Locate and identify every blood parasite.
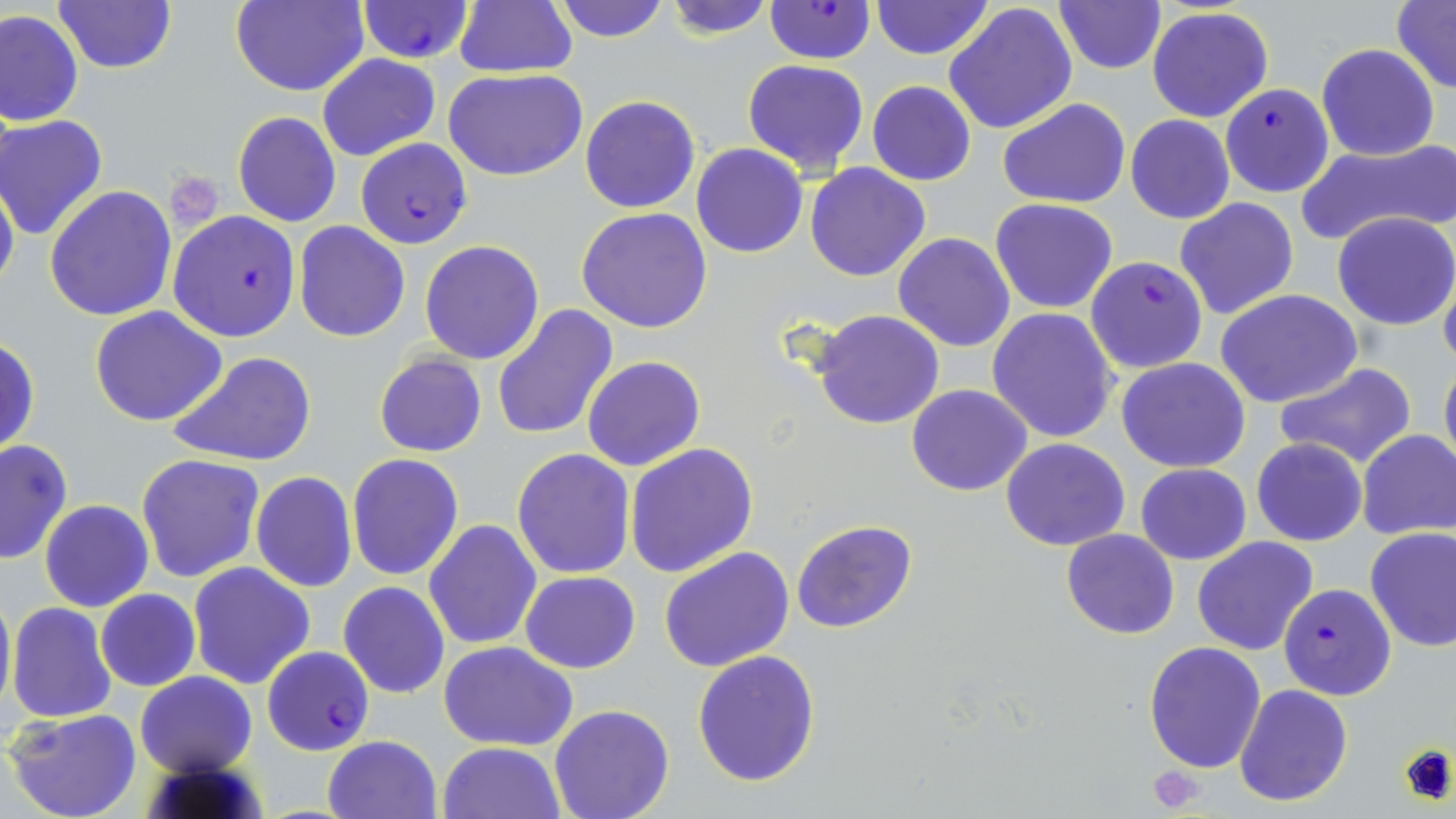
Approximate bounding boxes as (x1,y1)-(x2,y2) corner pairs in pixels.
Plasmodium falciparum-infected red blood cells: (356,2)-(474,62), (764,2)-(876,64), (1219,84)-(1334,198), (355,138)-(472,247), (168,210)-(301,341), (1085,255)-(1208,374), (1278,583)-(1395,700), (261,646)-(374,755).
No Plasmodium ovale, Plasmodium malariae, Plasmodium vivax, Babesia divergens, or Trypanosoma brucei observed.

Platelet locations: (1397,742)-(1456,805), (1147,765)-(1207,812). Uninfected red blood cell locations: (229,0)-(368,95), (552,0)-(671,42), (661,0)-(779,37), (1052,0)-(1165,74), (52,1)-(178,75), (452,1)-(578,78), (868,1)-(995,58), (1393,1)-(1456,93), (945,4)-(1077,135), (1146,6)-(1274,124), (0,10)-(84,127), (1316,44)-(1440,162), (316,53)-(439,162), (742,58)-(871,176), (445,66)-(589,181), (866,81)-(976,186), (580,95)-(700,213), (997,98)-(1132,207), (233,111)-(342,227), (1125,114)-(1235,224), (1,115)-(108,242), (1295,141)-(1454,248), (691,144)-(809,258), (805,162)-(930,282), (0,176)-(18,301), (45,186)-(177,322), (1174,196)-(1300,321), (990,198)-(1119,314), (576,207)-(712,333), (1332,211)-(1456,330), (295,222)-(411,341), (893,233)-(1016,352), (419,240)-(545,365), (1439,261)-(1456,376), (1217,290)-(1362,408), (492,303)-(621,440), (90,307)-(226,427), (811,308)-(945,430), (987,309)-(1118,444), (1,336)-(39,460), (167,351)-(318,467), (374,353)-(487,458), (584,356)-(705,472), (1116,357)-(1251,472), (1439,358)-(1456,478), (1273,363)-(1421,471), (907,383)-(1032,495), (593,387)-(736,546), (1356,428)-(1456,541), (1000,438)-(1130,550), (1251,438)-(1367,547), (0,439)-(73,565), (625,443)-(758,578), (513,448)-(635,578), (137,454)-(265,582), (346,454)-(464,581), (1136,463)-(1250,564), (251,473)-(357,591), (40,500)-(153,611), (424,519)-(541,651), (791,519)-(918,635), (1363,527)-(1456,652), (1061,528)-(1179,639), (1192,536)-(1321,656), (658,547)-(795,672), (187,561)-(316,690), (519,571)-(639,674), (0,581)-(16,722), (339,581)-(450,699), (96,589)-(200,692), (6,602)-(118,724), (438,640)-(579,751), (1143,640)-(1267,773), (692,648)-(822,787), (134,670)-(256,776), (1233,683)-(1354,806), (549,703)-(676,819), (5,708)-(143,819), (323,734)-(441,819), (439,742)-(564,818). Slide-level diagnosis: Plasmodium falciparum. Light microscopy. Thin blood smear. Image is 1456×819 pixels. Captured at 1000x magnification. One field of a larger specimen. May-Grünwald-Giemsa stain.